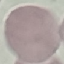

{
  "result": "no malaria parasites seen",
  "preparation": "thin blood film",
  "image_type": "automatically extracted cell patch, resized to 64 × 64 pixels",
  "capture": "smartphone camera at the microscope eyepiece",
  "stain": "Giemsa"
}